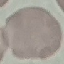
result: no malaria parasites seen
capture: smartphone through the microscope eyepiece
image_type: automatically extracted cell patch, resized to 64 × 64 pixels
preparation: thin smear
stain: Giemsa